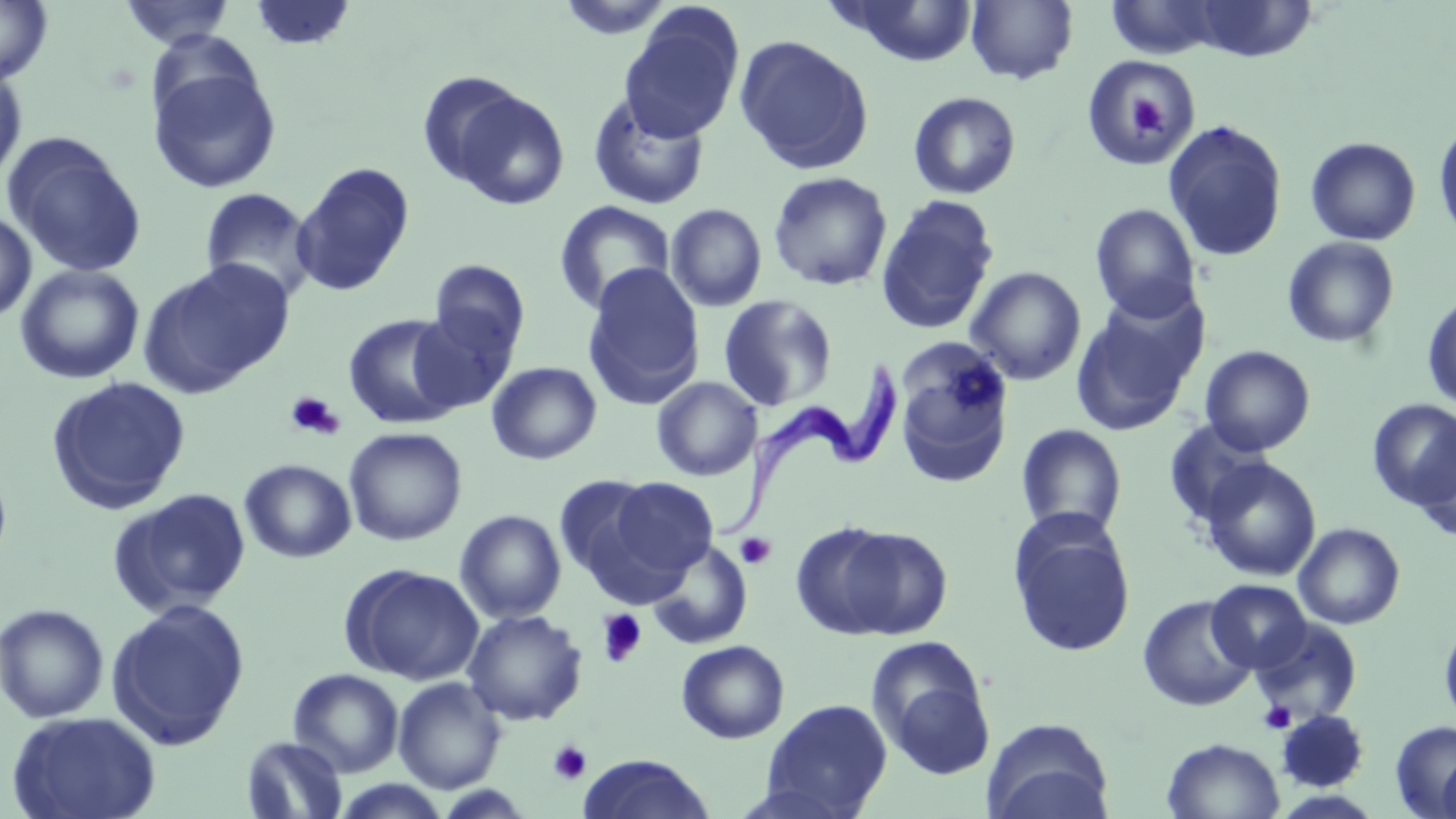

Approximate bounding boxes as (x1,y1)-(x2,y2) corner pairs in pixels. Platelet locations: (1123,91)-(1169,139), (284,390)-(344,441), (735,532)-(776,569), (597,609)-(647,667), (1259,701)-(1296,734), (548,740)-(592,785). Uninfected red blood cell locations: (556,0)-(677,41), (965,0)-(1079,85), (1106,0)-(1222,60), (0,1)-(54,87), (119,1)-(236,49), (249,1)-(356,50), (837,1)-(979,66), (1187,2)-(1317,61), (618,10)-(743,143), (734,34)-(874,174), (1082,55)-(1203,167), (147,62)-(282,195), (0,66)-(27,187), (417,71)-(528,186), (450,88)-(571,211), (587,91)-(710,210), (908,91)-(1021,199), (1433,119)-(1456,245), (1163,120)-(1288,262), (3,133)-(147,279), (1305,136)-(1421,246), (292,162)-(415,296), (768,171)-(893,291), (200,187)-(316,301), (665,193)-(895,301), (876,195)-(999,335), (553,201)-(675,315), (665,203)-(767,312), (1089,203)-(1202,322), (0,210)-(37,323), (1282,236)-(1401,349), (143,259)-(292,393), (429,260)-(530,358), (15,264)-(145,384), (582,264)-(705,409), (965,266)-(1086,385), (1071,290)-(1207,436), (1422,290)-(1456,413), (718,295)-(838,411), (408,308)-(517,414), (343,313)-(462,429), (893,339)-(1014,485), (1200,345)-(1316,455), (486,361)-(602,465), (46,376)-(192,513), (652,377)-(761,481), (1368,398)-(1456,510), (1163,418)-(1273,526), (1016,423)-(1127,538), (343,427)-(467,546), (1413,430)-(1456,542), (1201,458)-(1321,581), (0,459)-(13,577), (240,459)-(356,562), (554,475)-(659,582), (607,477)-(718,579), (112,488)-(251,616), (454,509)-(566,623), (1009,519)-(1136,658), (1293,522)-(1405,630), (827,525)-(953,639), (648,541)-(752,649), (342,563)-(485,685), (1206,579)-(1312,672), (1137,595)-(1258,712), (106,598)-(250,750), (0,602)-(109,724), (462,609)-(587,726), (1439,618)-(1456,733), (1249,619)-(1362,726), (866,638)-(990,761), (676,639)-(790,743), (288,668)-(404,777), (393,677)-(506,793), (761,698)-(893,817), (1276,709)-(1369,792), (6,711)-(162,819), (982,717)-(1114,819), (1390,719)-(1456,817), (240,735)-(348,819), (1162,737)-(1285,819), (1437,749)-(1456,819), (579,755)-(716,819), (332,778)-(453,819). Trypanosoma brucei locations: (723,355)-(900,539). Slide-level diagnosis: Trypanosoma brucei. Light microscopy. May-Grünwald-Giemsa stain. One field of a larger specimen. 1000x magnification. Thin blood smear. Image is 1456×819 pixels.